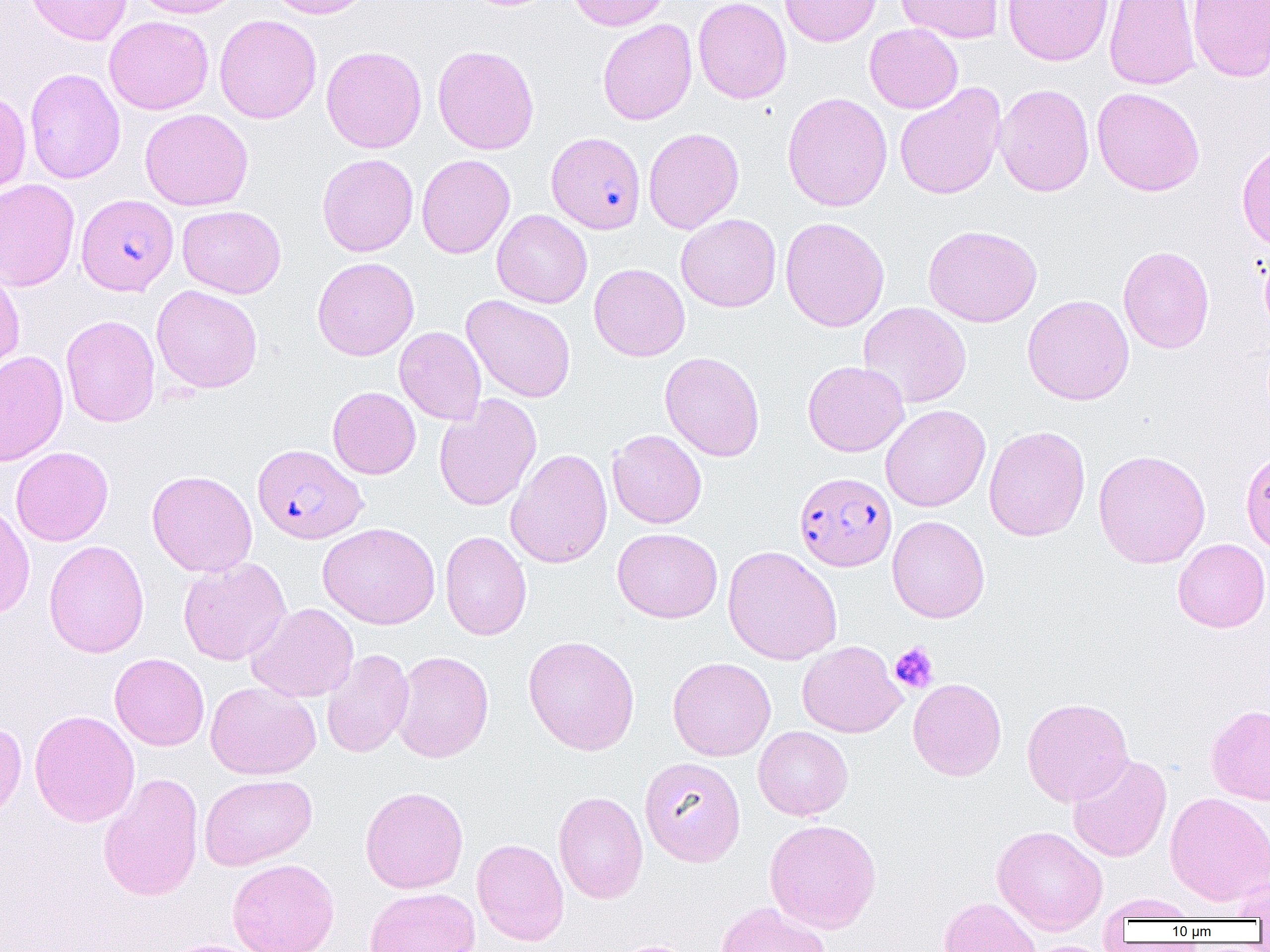
slide-level diagnosis = Plasmodium falciparum
platelet locations = approximate bounding boxes as named x1/y1/x2/y2 corners in pixels: (x1=889, y1=641, x2=938, y2=693)
field of view = one of a larger specimen
preparation = thin blood smear
Plasmodium falciparum-infected red blood cell locations = approximate bounding boxes as named x1/y1/x2/y2 corners in pixels: (x1=546, y1=132, x2=646, y2=234), (x1=76, y1=193, x2=178, y2=296), (x1=253, y1=444, x2=367, y2=544), (x1=794, y1=471, x2=896, y2=571)
magnification = 1000x
uninfected red blood cell locations = approximate bounding boxes as named x1/y1/x2/y2 corners in pixels: (x1=25, y1=0, x2=132, y2=46), (x1=131, y1=0, x2=244, y2=18), (x1=263, y1=0, x2=376, y2=19), (x1=567, y1=0, x2=672, y2=31), (x1=693, y1=0, x2=792, y2=104), (x1=780, y1=0, x2=881, y2=47), (x1=896, y1=0, x2=1003, y2=43), (x1=1003, y1=0, x2=1114, y2=66), (x1=1103, y1=0, x2=1201, y2=91), (x1=1186, y1=0, x2=1270, y2=82), (x1=214, y1=14, x2=322, y2=124), (x1=104, y1=15, x2=213, y2=115), (x1=597, y1=19, x2=697, y2=125), (x1=864, y1=23, x2=963, y2=114), (x1=321, y1=45, x2=427, y2=153), (x1=433, y1=45, x2=539, y2=155), (x1=24, y1=68, x2=126, y2=184), (x1=894, y1=83, x2=1006, y2=200), (x1=994, y1=83, x2=1094, y2=197), (x1=1092, y1=87, x2=1205, y2=196), (x1=0, y1=88, x2=31, y2=199), (x1=782, y1=92, x2=893, y2=212), (x1=140, y1=108, x2=253, y2=211), (x1=643, y1=127, x2=744, y2=234), (x1=1236, y1=140, x2=1270, y2=254), (x1=317, y1=154, x2=418, y2=257), (x1=417, y1=154, x2=515, y2=259), (x1=0, y1=178, x2=80, y2=291), (x1=177, y1=205, x2=286, y2=298), (x1=492, y1=209, x2=592, y2=308), (x1=676, y1=213, x2=781, y2=312), (x1=780, y1=217, x2=890, y2=332), (x1=923, y1=224, x2=1042, y2=327), (x1=1118, y1=245, x2=1215, y2=354), (x1=1259, y1=246, x2=1270, y2=339), (x1=312, y1=256, x2=419, y2=361), (x1=589, y1=263, x2=690, y2=361), (x1=0, y1=267, x2=24, y2=378), (x1=151, y1=284, x2=263, y2=394), (x1=1022, y1=294, x2=1134, y2=405), (x1=462, y1=295, x2=576, y2=403), (x1=858, y1=301, x2=972, y2=408), (x1=60, y1=314, x2=160, y2=427), (x1=394, y1=326, x2=486, y2=425), (x1=0, y1=351, x2=68, y2=466), (x1=660, y1=352, x2=765, y2=462), (x1=802, y1=360, x2=909, y2=457), (x1=327, y1=386, x2=421, y2=479), (x1=434, y1=394, x2=542, y2=512), (x1=880, y1=404, x2=990, y2=512), (x1=983, y1=425, x2=1090, y2=541), (x1=607, y1=429, x2=707, y2=528), (x1=11, y1=446, x2=113, y2=546), (x1=505, y1=448, x2=613, y2=569), (x1=1092, y1=449, x2=1211, y2=569), (x1=1240, y1=450, x2=1270, y2=555), (x1=146, y1=470, x2=258, y2=577), (x1=0, y1=502, x2=35, y2=620), (x1=887, y1=515, x2=990, y2=623), (x1=318, y1=522, x2=440, y2=629), (x1=612, y1=527, x2=722, y2=623), (x1=440, y1=530, x2=531, y2=640), (x1=1172, y1=538, x2=1270, y2=632), (x1=43, y1=540, x2=149, y2=658), (x1=722, y1=545, x2=843, y2=665), (x1=178, y1=557, x2=291, y2=666), (x1=246, y1=602, x2=359, y2=703), (x1=523, y1=634, x2=640, y2=756), (x1=797, y1=641, x2=906, y2=738), (x1=321, y1=648, x2=414, y2=758), (x1=391, y1=650, x2=494, y2=763), (x1=109, y1=652, x2=209, y2=751), (x1=667, y1=656, x2=776, y2=761), (x1=908, y1=677, x2=1007, y2=781), (x1=205, y1=681, x2=320, y2=780), (x1=1021, y1=697, x2=1133, y2=806), (x1=1206, y1=705, x2=1270, y2=805), (x1=29, y1=709, x2=140, y2=827), (x1=0, y1=720, x2=27, y2=824), (x1=753, y1=726, x2=853, y2=820), (x1=1067, y1=753, x2=1171, y2=863), (x1=639, y1=756, x2=746, y2=866), (x1=98, y1=772, x2=204, y2=901), (x1=199, y1=773, x2=317, y2=870), (x1=360, y1=786, x2=469, y2=894), (x1=553, y1=790, x2=648, y2=904), (x1=1164, y1=792, x2=1270, y2=906), (x1=764, y1=819, x2=882, y2=933), (x1=992, y1=824, x2=1108, y2=935), (x1=472, y1=838, x2=569, y2=945), (x1=227, y1=858, x2=340, y2=952), (x1=1227, y1=875, x2=1270, y2=921), (x1=364, y1=887, x2=480, y2=952), (x1=1099, y1=894, x2=1201, y2=922), (x1=938, y1=897, x2=1041, y2=951), (x1=715, y1=901, x2=832, y2=952), (x1=160, y1=939, x2=266, y2=952), (x1=611, y1=939, x2=702, y2=952)
image size = 1270×952 pixels
modality = light microscopy